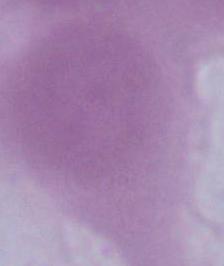

magnification: 1000x
modality: micrograph
identification: erythrocyte